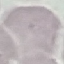
Malaria status: uninfected. Photographed with a smartphone camera at the microscope eyepiece. Cell patch, automatically extracted from a larger field of view and resized to 64 × 64 pixels. Thin smear of blood. Giemsa stain.